Report the malaria status of this cell.
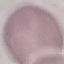

Uninfected.

Summary:
  - Preparation: thin smear
  - Capture: smartphone camera at the microscope eyepiece
  - Stain: Giemsa
  - Image type: automatically extracted cell patch, resized to 64 × 64 pixels